Assess this cell for malaria.
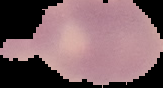

It is uninfected.

Summary:
  - Preparation: thin blood film
  - Image type: segmented cell region on a black background
  - Image size: 163×88 pixels